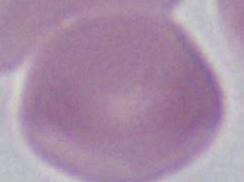
An erythrocyte is seen. Photomicrograph. Captured at 1000x magnification.